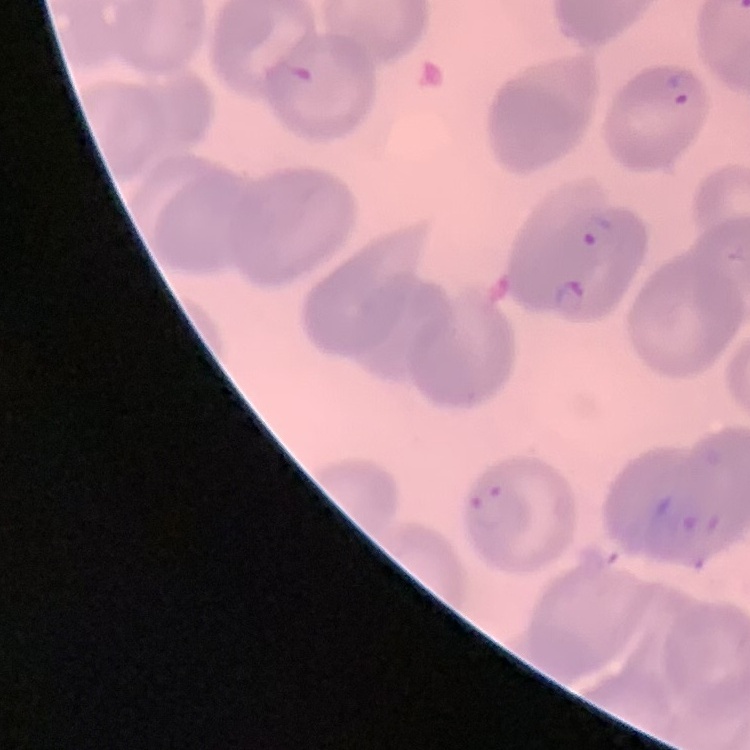

red blood cell morphology = no rouleaux formation
preparation = thin blood smear
image type = square crop of a larger photomicrograph
stain = Field's or Giemsa